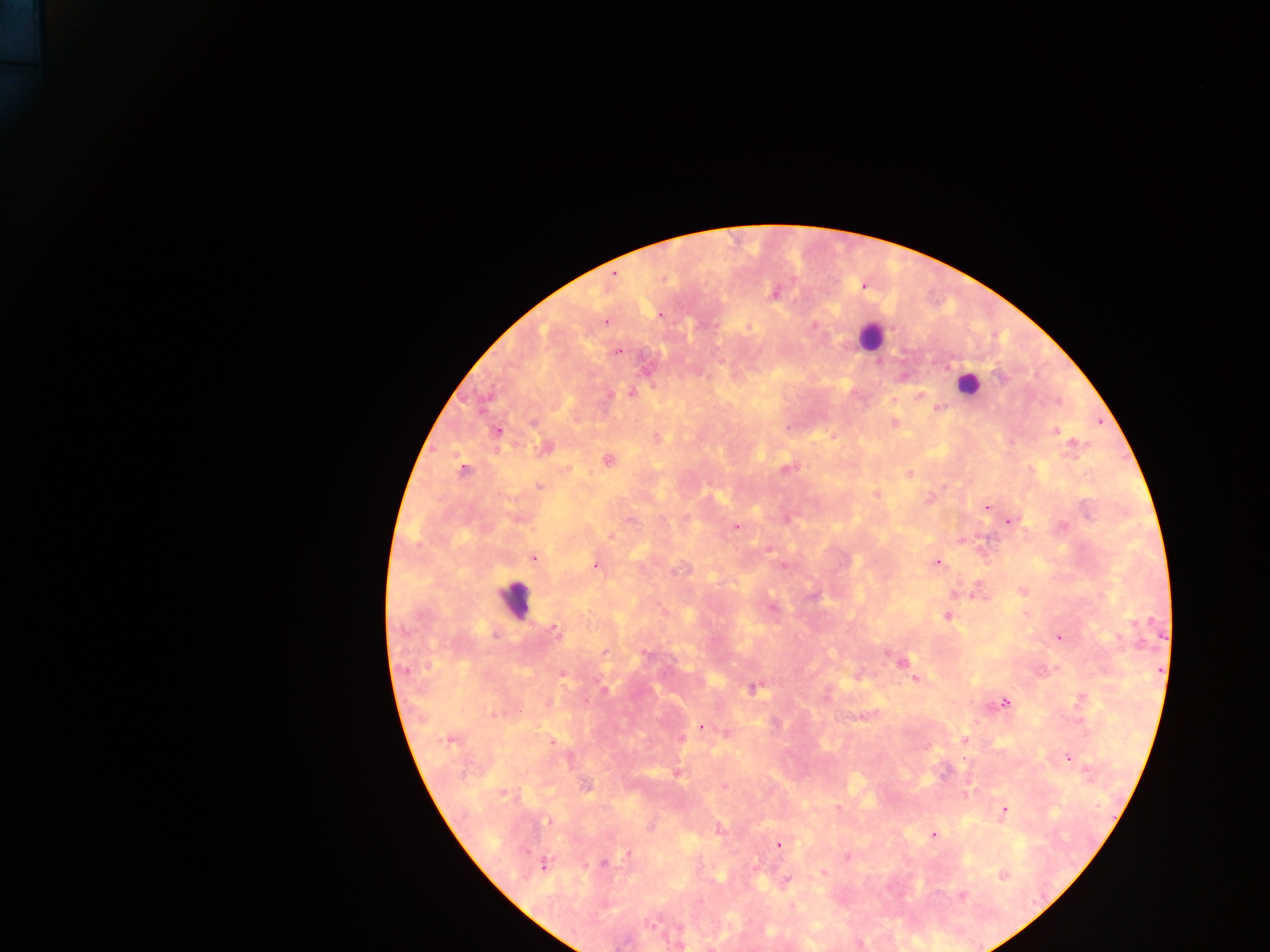
Approximate centers as (x, y) in pixels.
Summary:
  - Malaria parasite locations: (774, 292), (660, 315), (605, 322), (749, 326), (814, 326), (617, 351), (1000, 377), (631, 393), (920, 395), (939, 408), (532, 421), (894, 422), (1055, 430), (497, 432), (658, 438), (1075, 444), (544, 448), (608, 461), (788, 468), (568, 469), (462, 470), (909, 474), (539, 485), (876, 494), (931, 498), (987, 506), (1011, 521), (737, 526), (1063, 526), (610, 537), (534, 557), (937, 563), (596, 565), (812, 595), (948, 616), (555, 629), (1060, 637), (605, 652), (886, 652), (646, 654), (901, 662), (563, 675), (916, 678), (754, 688), (604, 689), (1005, 703), (494, 714), (700, 726), (450, 740), (965, 740), (552, 742), (1067, 757), (678, 773), (585, 786), (725, 786), (503, 794), (839, 808), (1004, 810), (548, 821), (719, 830), (934, 835), (778, 846), (630, 854), (848, 857), (543, 864), (603, 864), (824, 872), (1004, 875), (786, 880), (962, 896), (793, 906)
  - Leukocyte locations: (869, 338), (966, 384), (515, 599)
  - Field of view: single
  - Country: Ghana
  - Preparation: thick blood smear
  - Capture: mobile-phone photograph through a microscope
  - Image size: 1270×952 pixels